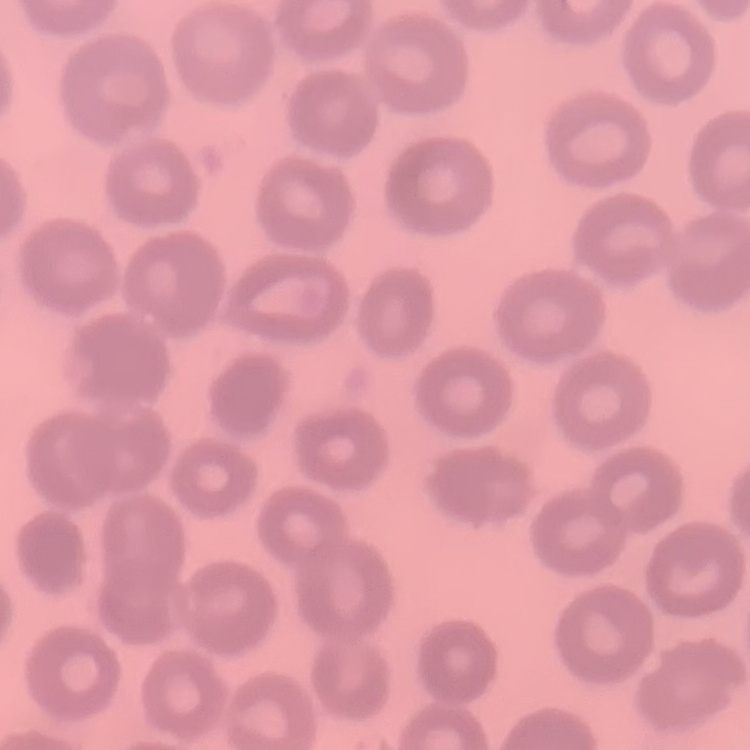
erythrocyte morphology = no rouleaux formation
preparation = thin peripheral smear
image type = one tile cut from a larger photomicrograph
stain = Field's or Giemsa